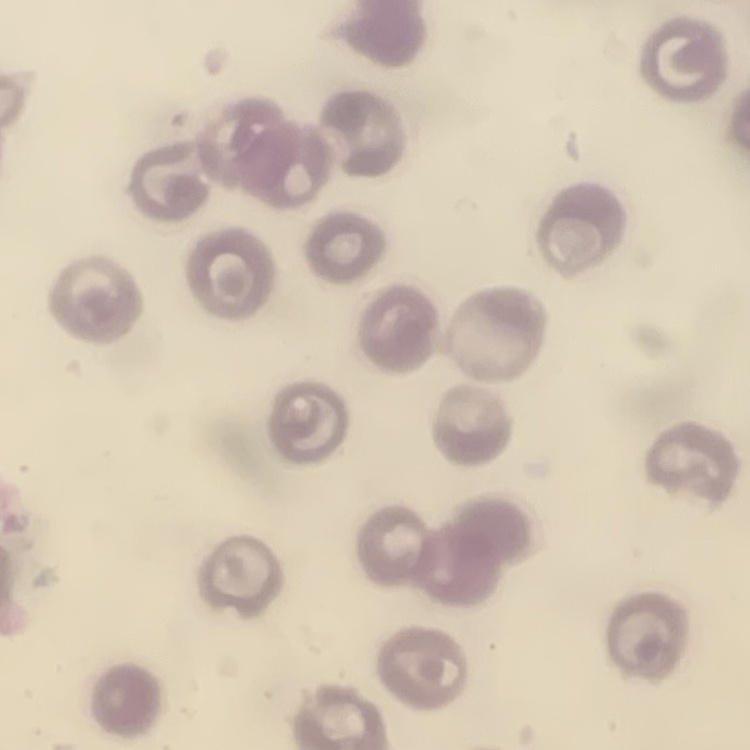
Summary:
  - Erythrocyte morphology: no rouleaux formation
  - Image type: one tile cut from a larger photomicrograph
  - Stain: Field's or Giemsa
  - Preparation: thin blood smear